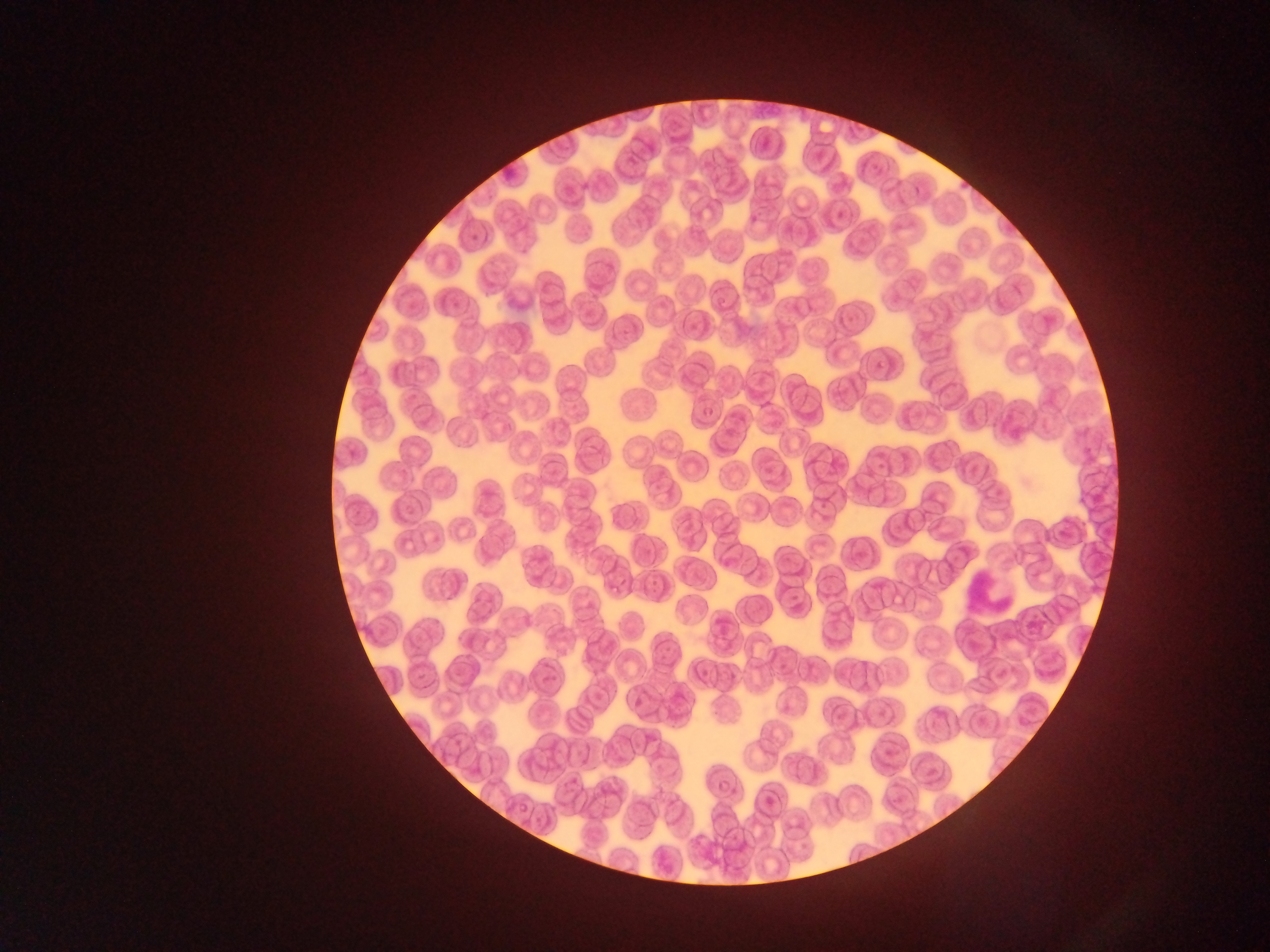 Approximate bounding boxes as {left, top, right, bottom} in pixels. Leukocyte locations: {964, 573, 1011, 612}. Image is 1270×952 pixels. Sample from Ghana. Thin blood smear. One field of view. Mobile-phone photograph taken through the microscope.